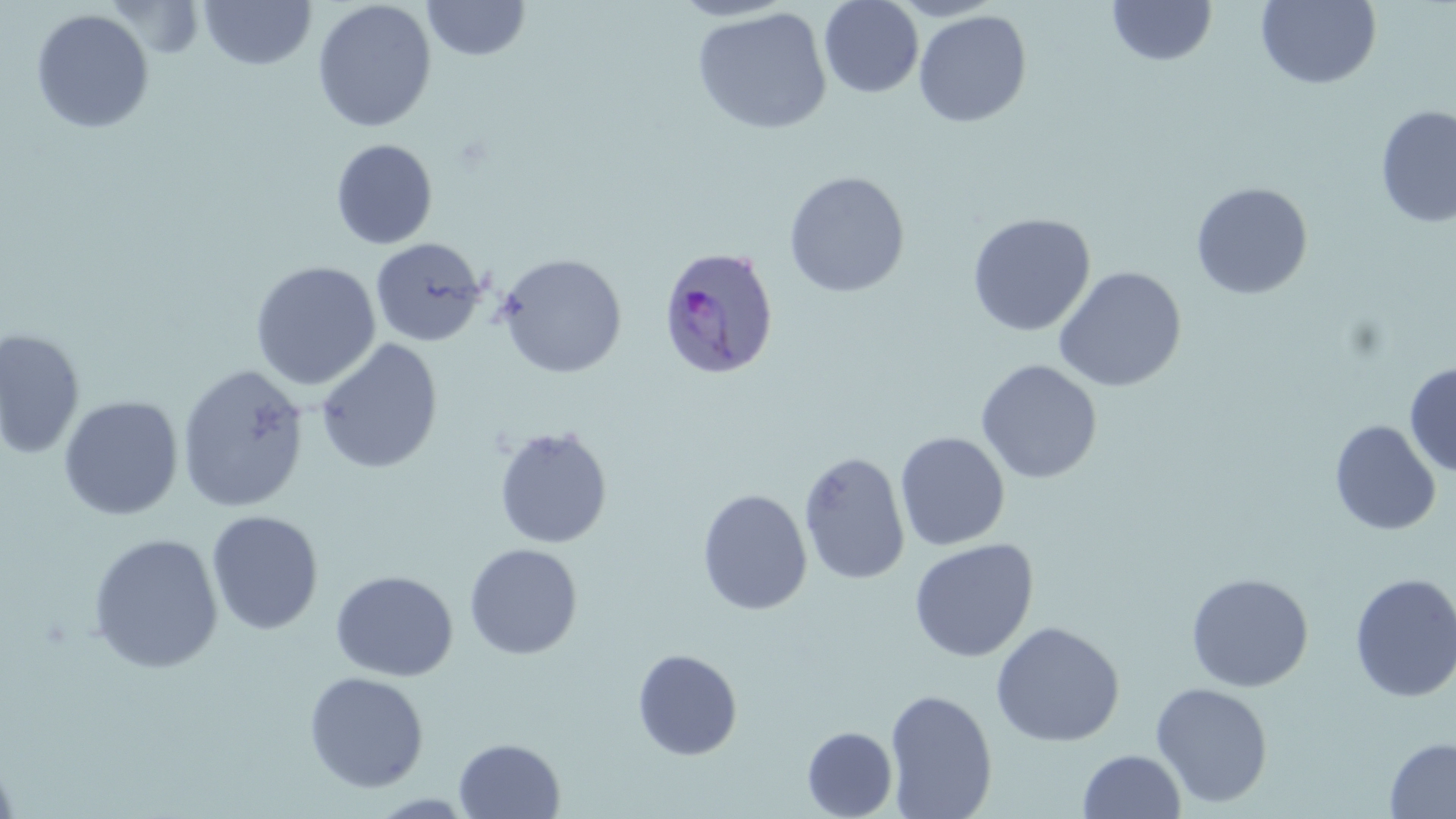
Summary:
  - Coordinate format: approximate bounding boxes as [x1, y1, x2, y2] in pixels
  - Plasmodium ovale-infected red blood cell locations: [657, 246, 780, 381]
  - Uninfected red blood cell locations: [199, 0, 317, 70], [312, 0, 437, 133], [819, 0, 923, 98], [1107, 0, 1218, 66], [1256, 0, 1382, 89], [422, 1, 531, 61], [692, 7, 832, 135], [30, 9, 154, 134], [913, 10, 1032, 128], [1376, 105, 1456, 229], [330, 138, 438, 250], [784, 170, 910, 298], [1190, 182, 1313, 299], [967, 213, 1096, 337], [370, 237, 486, 347], [496, 253, 627, 378], [250, 261, 381, 390], [1053, 266, 1187, 392], [0, 327, 86, 461], [315, 339, 443, 474], [975, 359, 1103, 484], [1404, 361, 1456, 477], [176, 364, 309, 514], [59, 396, 183, 521], [1329, 419, 1442, 536], [493, 425, 614, 549], [895, 432, 1010, 551], [798, 450, 911, 586], [697, 488, 812, 616], [206, 511, 324, 635], [88, 533, 223, 674], [908, 538, 1038, 663], [464, 543, 583, 660], [330, 570, 458, 682], [1185, 572, 1314, 692], [1349, 572, 1456, 703], [990, 621, 1125, 747], [632, 648, 743, 761], [304, 671, 429, 793], [1151, 682, 1273, 808], [884, 688, 998, 818], [802, 726, 898, 818], [1384, 736, 1456, 819], [453, 738, 565, 818], [1077, 749, 1186, 818], [0, 750, 22, 819]
  - Slide-level diagnosis: Plasmodium ovale
  - Stain: May-Grünwald-Giemsa
  - Preparation: thin blood smear
  - Magnification: 1000x
  - Image size: 1456×819 pixels
  - Field of view: single
  - Modality: optical microscopy